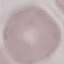 Malaria status: uninfected. Giemsa stain. Thin blood film. Cell patch, automatically extracted from a larger field of view and resized to 64 × 64 pixels. Photographed with a smartphone camera at the microscope eyepiece.